Locate and identify every blood parasite.
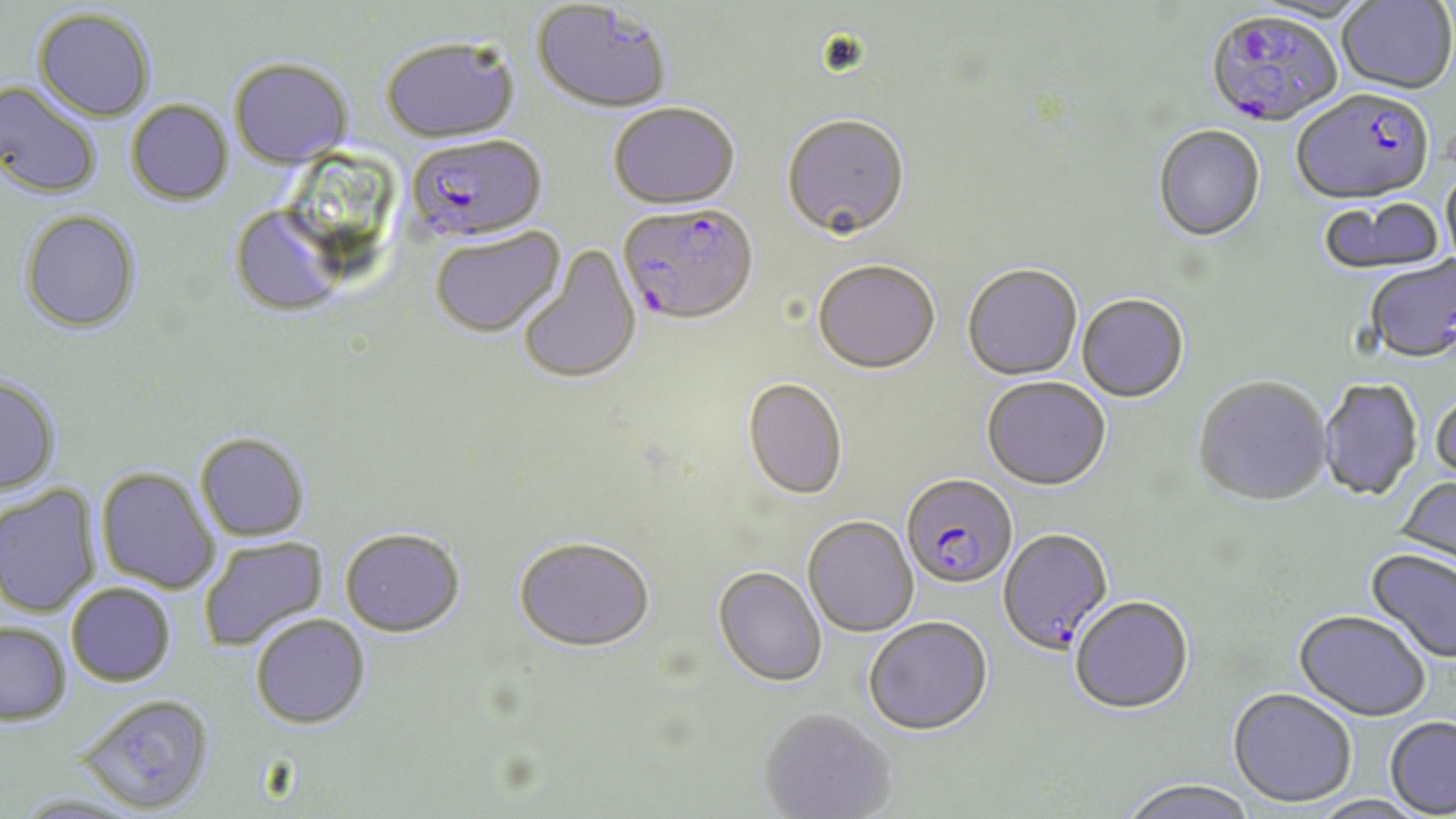
Approximate bounding boxes as [x1, y1, x2, y2] in pixels.
Plasmodium falciparum-infected red blood cells: [1206, 12, 1342, 130], [1292, 92, 1436, 208], [406, 134, 546, 245], [618, 204, 757, 327], [901, 474, 1018, 590], [997, 528, 1114, 657].
No Plasmodium ovale, Plasmodium malariae, Plasmodium vivax, Babesia divergens, or Trypanosoma brucei observed.

Uninfected red blood cell locations: [1337, 0, 1456, 96], [1247, 1, 1374, 26], [531, 2, 673, 115], [32, 8, 155, 123], [380, 36, 519, 142], [228, 57, 353, 168], [0, 82, 101, 199], [126, 100, 233, 206], [608, 102, 740, 210], [781, 113, 911, 241], [1153, 127, 1266, 244], [1441, 166, 1456, 272], [1317, 198, 1444, 279], [229, 206, 346, 317], [19, 210, 141, 334], [431, 227, 566, 339], [518, 244, 641, 385], [1364, 258, 1456, 366], [812, 261, 941, 376], [962, 266, 1082, 382], [1077, 296, 1189, 404], [0, 376, 61, 496], [741, 378, 848, 501], [982, 378, 1111, 492], [1193, 378, 1332, 508], [1318, 379, 1423, 503], [1431, 391, 1456, 486], [194, 432, 311, 542], [96, 467, 220, 595], [1393, 476, 1456, 578], [0, 485, 100, 617], [803, 516, 919, 637], [339, 527, 465, 637], [198, 536, 330, 654], [514, 537, 656, 654], [1363, 548, 1456, 665], [713, 567, 827, 688], [66, 583, 175, 687], [1070, 598, 1193, 716], [1293, 611, 1431, 723], [250, 613, 370, 729], [863, 617, 993, 737], [0, 621, 72, 725], [1227, 689, 1356, 809], [77, 693, 214, 814], [759, 709, 896, 818], [1384, 716, 1456, 817], [1119, 780, 1259, 819], [12, 793, 142, 819], [1308, 796, 1433, 819]. Slide-level diagnosis: Plasmodium falciparum. Optical microscopy. Image is 1456×819 pixels. May-Grünwald-Giemsa-stained preparation. One field of a larger specimen. Captured at 1000x magnification. Thin blood film.